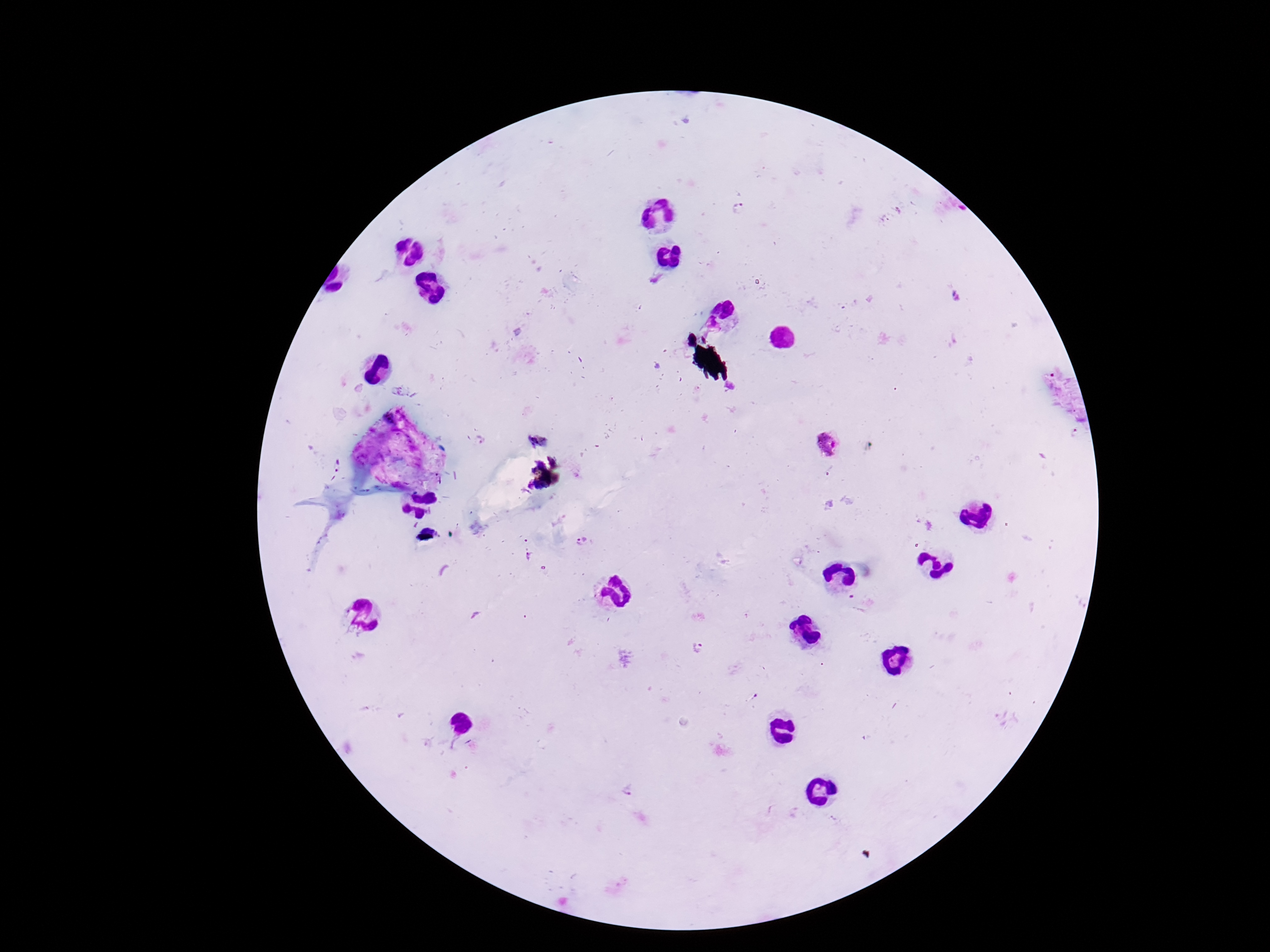
Approximate object centers, in pixels from the top-left corner.
Summary:
  - Plasmodium parasite locations: (x=739, y=210), (x=479, y=441), (x=826, y=444), (x=335, y=462), (x=581, y=541), (x=527, y=557), (x=694, y=648), (x=631, y=789)
  - Capture: smartphone camera through the microscope eyepiece
  - Field of view: single
  - Image size: 1270×952 pixels
  - Magnification: 100x
  - Preparation: thick peripheral-blood smear
  - Stain: Giemsa
  - Patient malaria status: infected